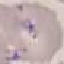
result = negative for malaria parasites
capture = smartphone through the microscope eyepiece
preparation = thin blood smear
stain = Giemsa
image type = automatically extracted cell patch, resized to 64 × 64 pixels